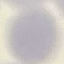

Summary:
  - Result: no malaria parasites detected
  - Preparation: thin blood smear
  - Image type: cell patch, automatically extracted from a larger field of view and resized to 64 × 64 pixels
  - Stain: Giemsa
  - Capture: smartphone camera at the microscope eyepiece